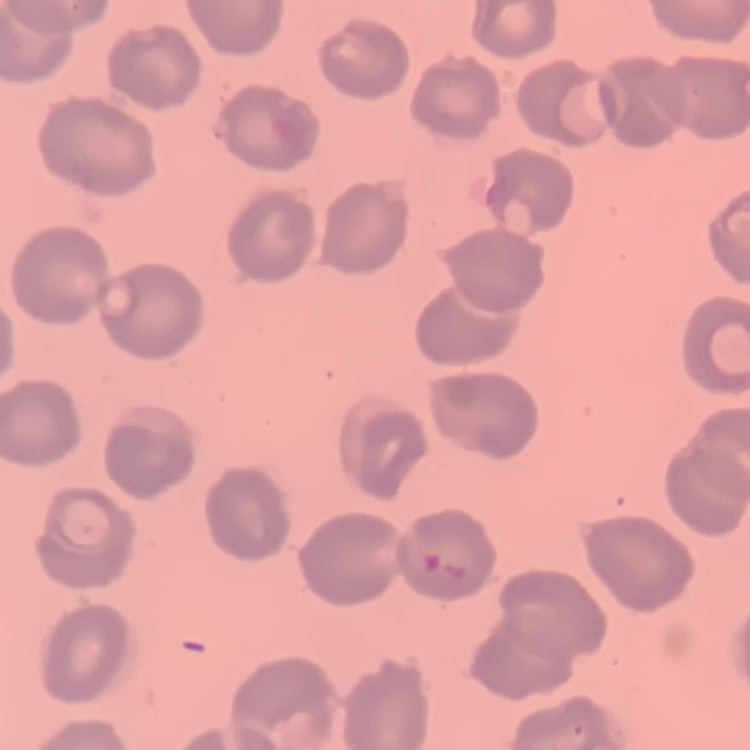
The red blood cells show no rouleaux formation. Stained with either Field's or Giemsa. Thin blood smear. Square crop of a larger photomicrograph.